Locate cells.
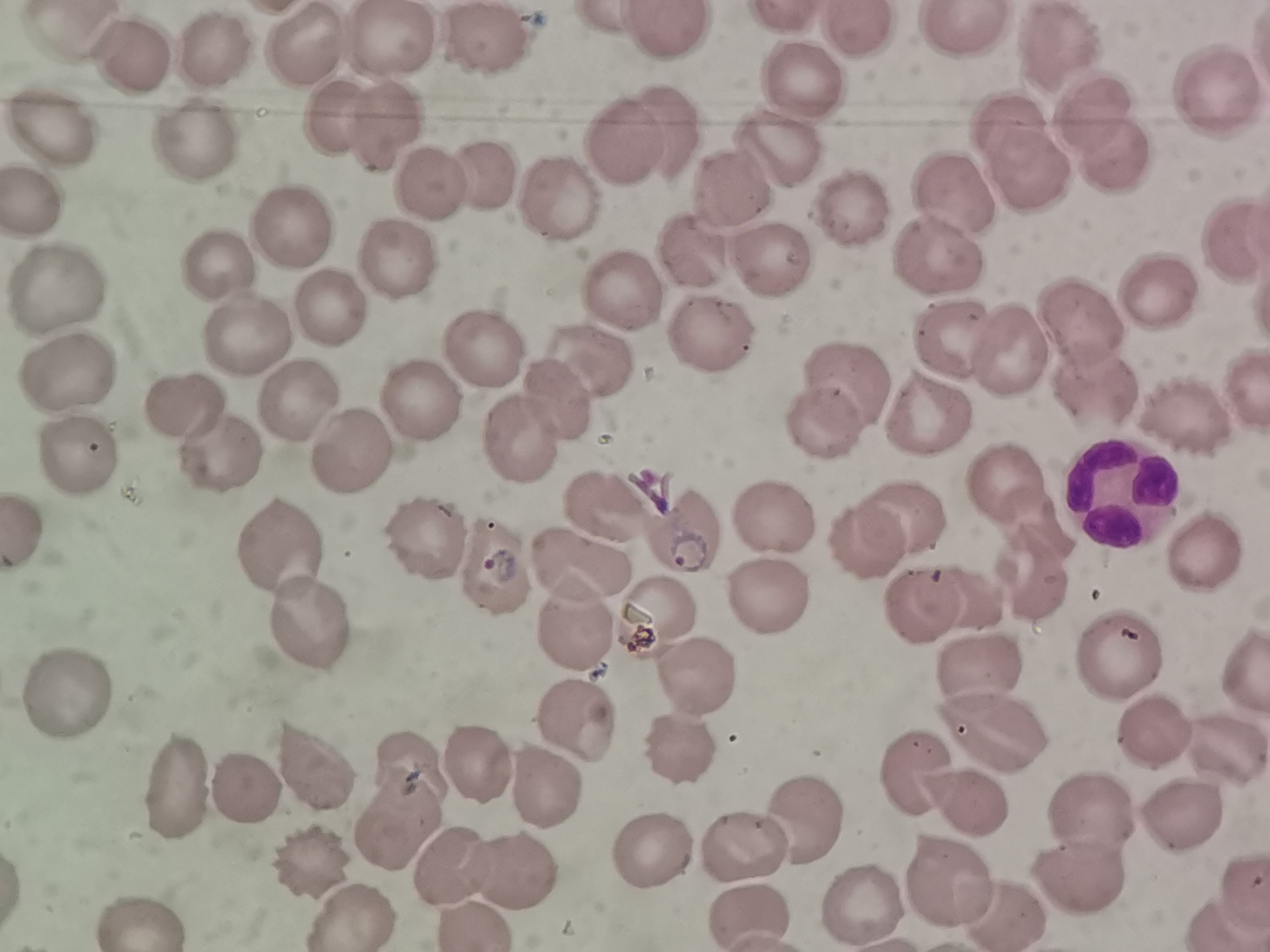

Approximate object centers, in pixels from the top-left corner.
Cells: (x=84, y=28), (x=854, y=30), (x=956, y=33), (x=661, y=39), (x=390, y=42), (x=311, y=44), (x=488, y=49), (x=1059, y=54), (x=213, y=56), (x=126, y=64), (x=805, y=76), (x=1214, y=98), (x=1092, y=109), (x=328, y=115), (x=378, y=121), (x=1010, y=126), (x=662, y=127), (x=49, y=130), (x=182, y=146), (x=628, y=146), (x=775, y=152), (x=1109, y=155), (x=1029, y=176), (x=488, y=177), (x=433, y=188), (x=950, y=190), (x=731, y=191), (x=38, y=202), (x=851, y=203), (x=558, y=206), (x=294, y=237), (x=1234, y=242), (x=939, y=251), (x=406, y=254), (x=221, y=265), (x=769, y=266), (x=62, y=286), (x=1165, y=288), (x=623, y=301), (x=331, y=311), (x=1082, y=320), (x=244, y=336), (x=708, y=336), (x=958, y=336), (x=478, y=345), (x=1009, y=350), (x=598, y=364), (x=840, y=370), (x=70, y=378), (x=296, y=395), (x=418, y=396), (x=1092, y=397), (x=556, y=400), (x=180, y=406), (x=1183, y=410), (x=925, y=411), (x=821, y=421), (x=510, y=435), (x=208, y=449), (x=342, y=452), (x=76, y=459), (x=1004, y=481), (x=1111, y=488), (x=603, y=507), (x=901, y=510), (x=763, y=515), (x=1036, y=524), (x=683, y=534), (x=423, y=536), (x=864, y=541), (x=287, y=549), (x=1203, y=552), (x=576, y=568), (x=502, y=569), (x=1018, y=577), (x=963, y=594), (x=763, y=596), (x=660, y=609), (x=922, y=609), (x=312, y=621), (x=576, y=627), (x=1108, y=654), (x=979, y=667), (x=691, y=679), (x=68, y=684), (x=1148, y=719), (x=578, y=721), (x=989, y=729), (x=1221, y=734), (x=678, y=738), (x=480, y=761), (x=312, y=762), (x=412, y=764), (x=908, y=767), (x=546, y=782), (x=188, y=788), (x=240, y=792), (x=965, y=798), (x=1094, y=802), (x=1176, y=809), (x=805, y=824), (x=405, y=825), (x=654, y=844), (x=743, y=851), (x=318, y=853), (x=459, y=868), (x=513, y=868), (x=1073, y=870), (x=944, y=885), (x=1239, y=885), (x=1002, y=900), (x=864, y=904), (x=348, y=912), (x=750, y=914), (x=138, y=917).

{
  "preparation": "thin blood film",
  "capture": "smartphone camera at the microscope eyepiece",
  "stain": "Giemsa",
  "image_size": "1270×952 pixels",
  "field_of_view": "single"
}